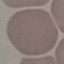

result = no malaria parasites seen
stain = Giemsa
preparation = thin smear
image type = cell patch, automatically extracted from a larger field of view and resized to 64 × 64 pixels
capture = smartphone through the microscope eyepiece